Identify the blood parasite species.
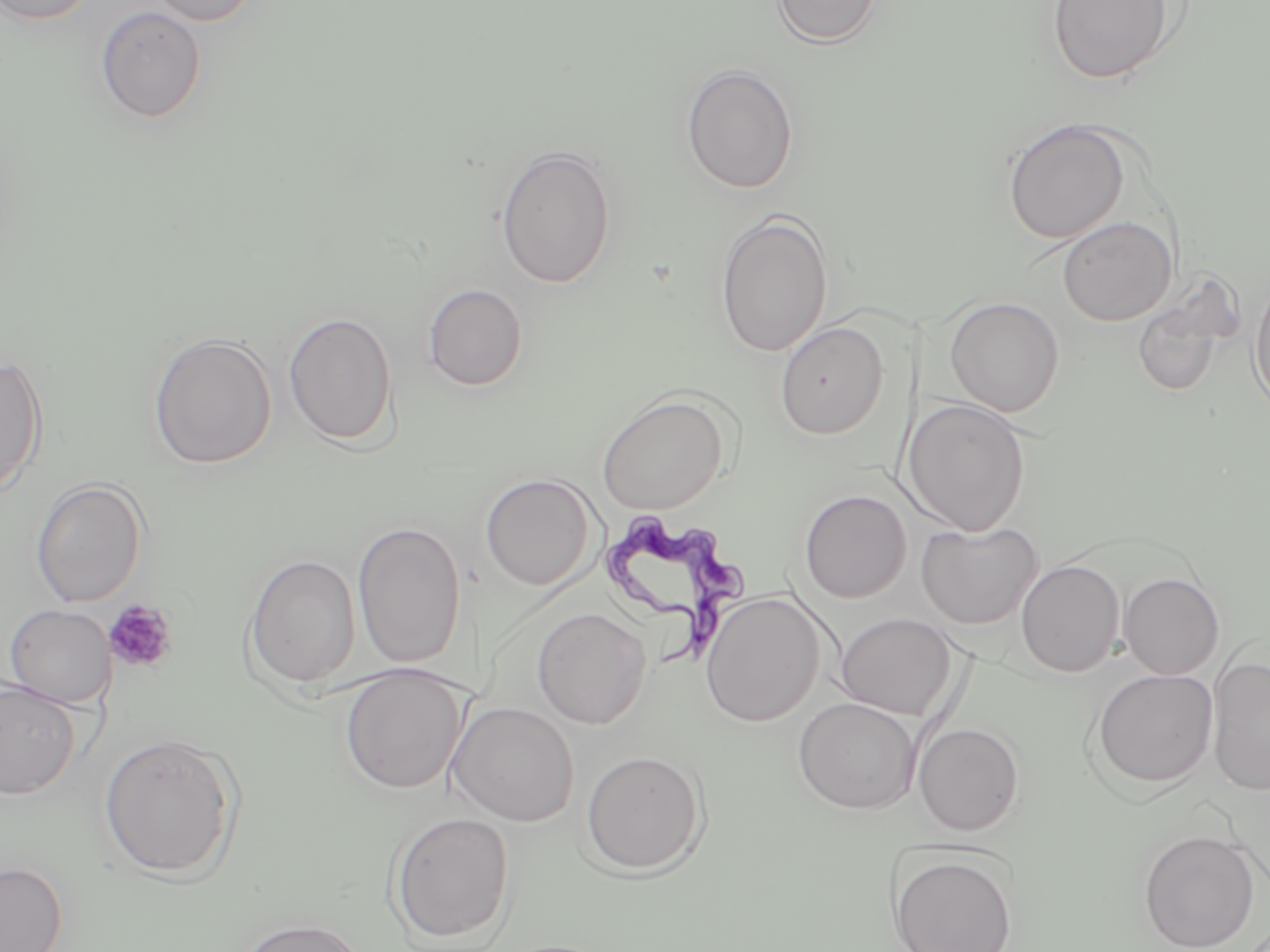

Trypanosoma brucei.

Approximate bounding boxes as (x1,y1)-(x2,y2) corner pairs in pixels. Trypanosoma brucei locations: (603,516)-(752,668). Platelet locations: (103,599)-(179,674). Uninfected red blood cell locations: (144,0)-(261,27), (771,0)-(883,48), (1046,0)-(1177,85), (0,1)-(99,27), (95,5)-(208,125), (680,64)-(799,194), (1001,118)-(1131,244), (495,144)-(617,289), (714,211)-(833,358), (1057,216)-(1177,326), (1248,271)-(1270,416), (423,283)-(528,391), (1130,290)-(1235,397), (944,297)-(1064,417), (283,311)-(398,448), (775,321)-(889,439), (147,332)-(278,470), (0,353)-(49,500), (597,392)-(729,515), (906,400)-(1031,536), (479,473)-(597,590), (31,478)-(148,608), (798,489)-(911,603), (352,520)-(467,670), (916,521)-(1043,629), (244,553)-(361,691), (1016,559)-(1124,677), (1118,572)-(1224,679), (700,591)-(825,727), (4,603)-(116,709), (532,608)-(652,729), (835,613)-(958,720), (1207,654)-(1270,798), (339,665)-(465,795), (1090,668)-(1219,789), (0,680)-(82,801), (447,686)-(481,822), (793,697)-(922,814), (457,701)-(581,828), (913,722)-(1025,836), (99,732)-(241,881), (580,748)-(709,876), (388,810)-(515,947), (1137,828)-(1260,951), (888,851)-(1018,951), (0,861)-(68,952), (232,916)-(370,952). Optical microscopy. 1000x magnification. Thin blood film. Image is 1270×952 pixels. May-Grünwald-Giemsa stain. One field of a larger specimen.